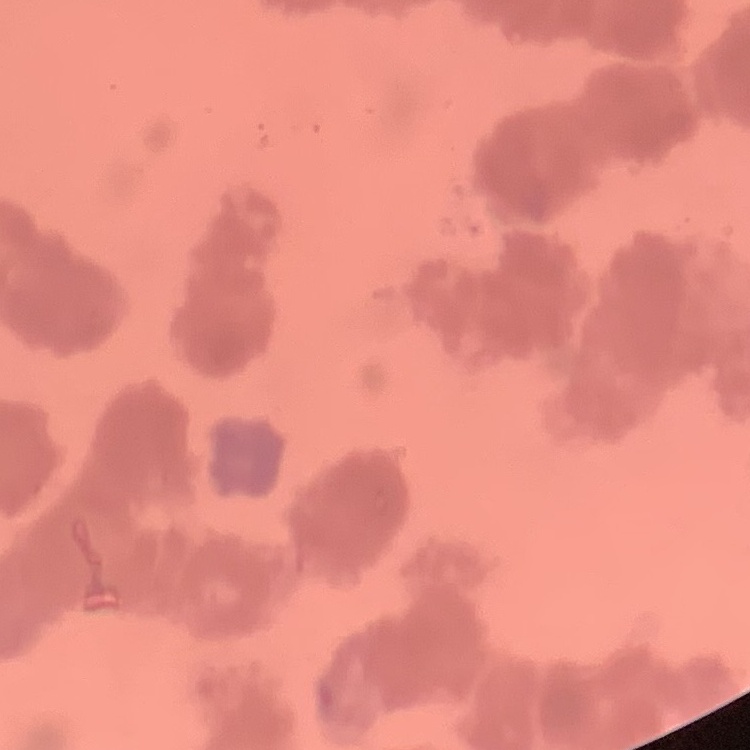
red_blood_cell_morphology: rouleaux formation
stain: Field's or Giemsa
preparation: thin blood film
image_type: one tile cut from a larger photomicrograph